Locate every blood parasite and identify its species.
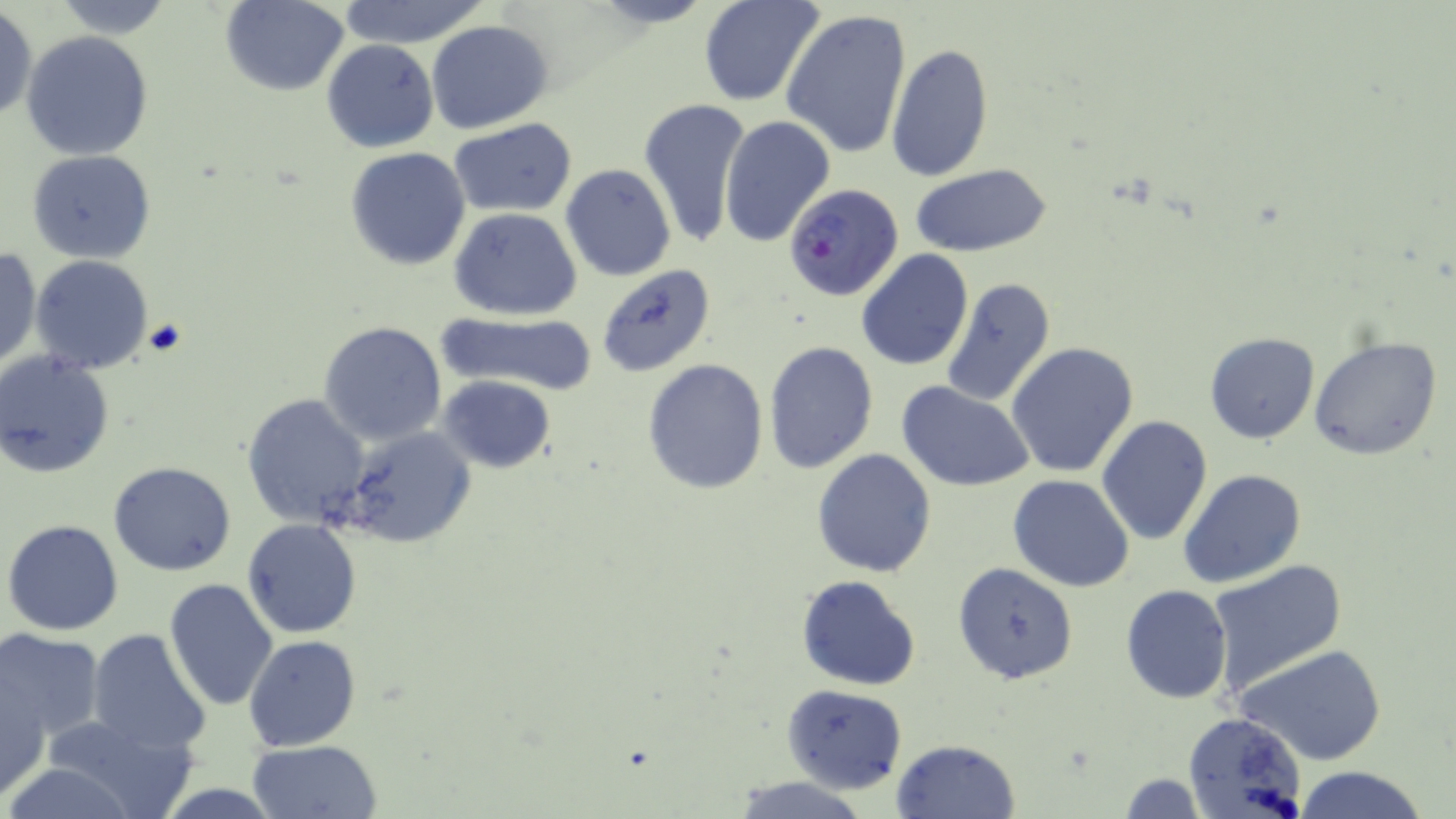
Approximate bounding boxes as [x1, y1, x2, y2] in pixels.
Plasmodium falciparum-infected red blood cells: [783, 183, 905, 303].
No Plasmodium ovale, Plasmodium malariae, Plasmodium vivax, Babesia divergens, or Trypanosoma brucei observed.

slide-level diagnosis = Plasmodium falciparum
modality = optical microscopy
stain = May-Grünwald-Giemsa
field of view = single
preparation = thin blood smear
image size = 1456×819 pixels
uninfected red blood cell locations = approximate bounding boxes as [x1, y1, x2, y2] in pixels: [48, 0, 178, 38], [698, 0, 823, 107], [220, 1, 350, 96], [333, 1, 493, 48], [1, 7, 37, 123], [780, 10, 913, 161], [427, 19, 552, 133], [22, 30, 154, 160], [321, 39, 439, 153], [886, 42, 993, 183], [639, 96, 752, 251], [719, 116, 834, 249], [448, 118, 579, 218], [346, 147, 471, 269], [27, 149, 156, 264], [911, 162, 1052, 257], [560, 163, 676, 283], [450, 207, 583, 319], [0, 248, 42, 371], [856, 250, 973, 371], [30, 255, 156, 374], [596, 265, 716, 377], [941, 278, 1056, 407], [437, 310, 598, 395], [320, 321, 448, 447], [1203, 333, 1320, 444], [1308, 335, 1444, 461], [763, 342, 879, 473], [1006, 343, 1139, 477], [0, 349, 115, 477], [642, 358, 769, 494], [438, 375, 556, 474], [899, 383, 1035, 492], [242, 392, 371, 528], [1097, 415, 1213, 544], [339, 426, 476, 550], [811, 448, 937, 578], [108, 461, 235, 575], [1178, 469, 1307, 589], [1008, 474, 1135, 592], [242, 518, 362, 638], [4, 519, 125, 636], [1205, 559, 1348, 696], [951, 561, 1079, 683], [796, 575, 921, 691], [163, 579, 280, 711], [1120, 585, 1232, 703], [0, 629, 105, 746], [86, 629, 211, 756], [244, 635, 361, 750], [1236, 642, 1387, 767], [0, 677, 50, 801], [782, 684, 908, 793], [41, 710, 199, 819], [1181, 711, 1308, 819], [249, 739, 382, 819], [890, 739, 1021, 819], [1295, 765, 1429, 819], [1117, 772, 1207, 817], [731, 776, 872, 818]
magnification = 1000x